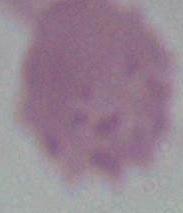
Photomicrograph. An erythrocyte is shown. Captured at 1000x magnification.